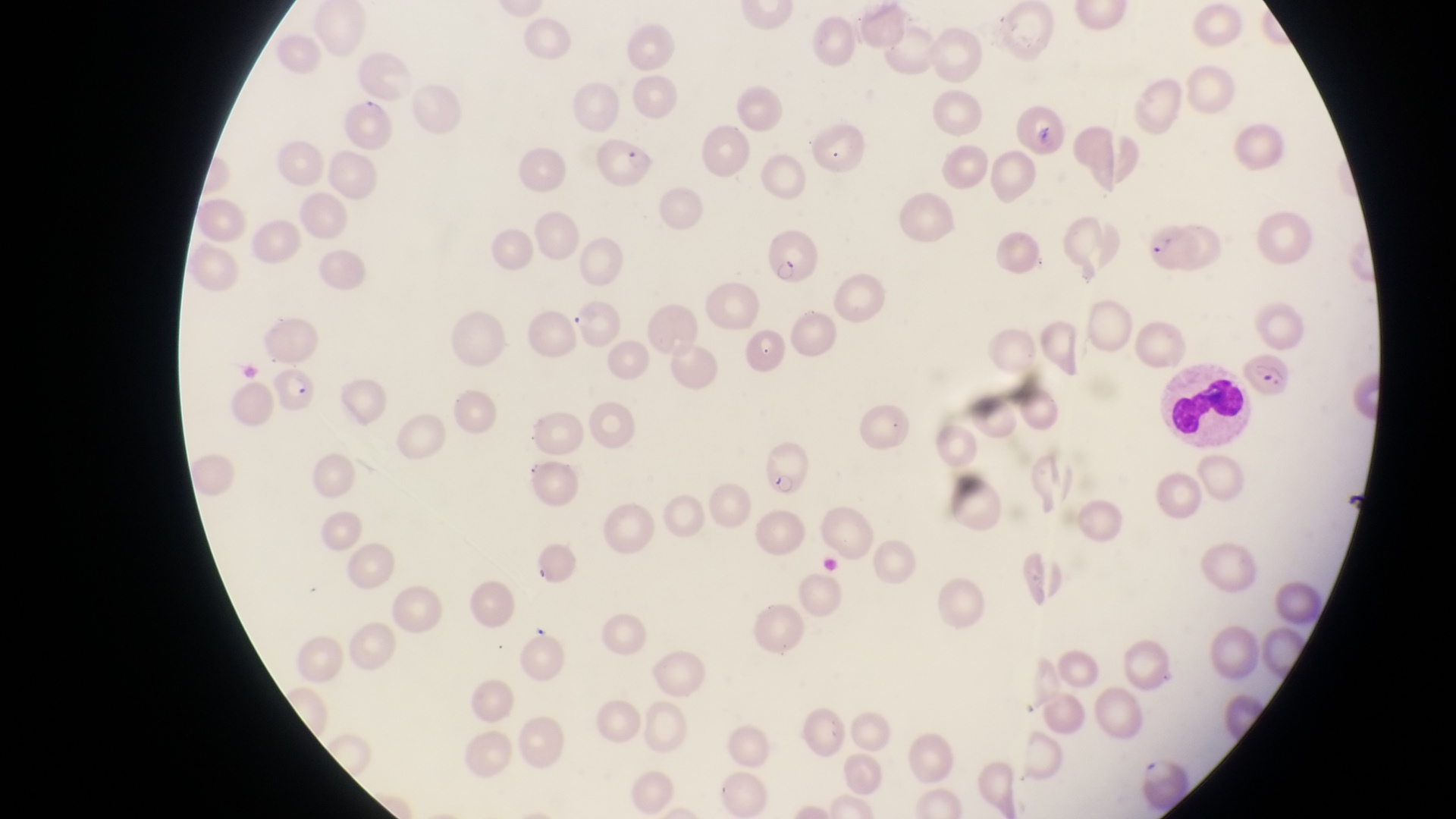
Approximate bounding boxes as [left, top, right, bottom] in pixels.
Summary:
  - Parasitised red blood cell locations: [597, 133, 660, 193], [1145, 222, 1201, 274], [764, 227, 825, 286], [1238, 347, 1296, 399], [264, 360, 324, 419], [755, 435, 814, 501]
  - Leukocyte locations: [1165, 359, 1251, 445]
  - Country: Uganda
  - Field of view: single
  - Image size: 1456×819 pixels
  - Preparation: thin blood smear
  - Capture: smartphone photograph through the eyepiece of an Olympus CX-23 microscope
  - Magnification: 1000x